Name the blood parasite species.
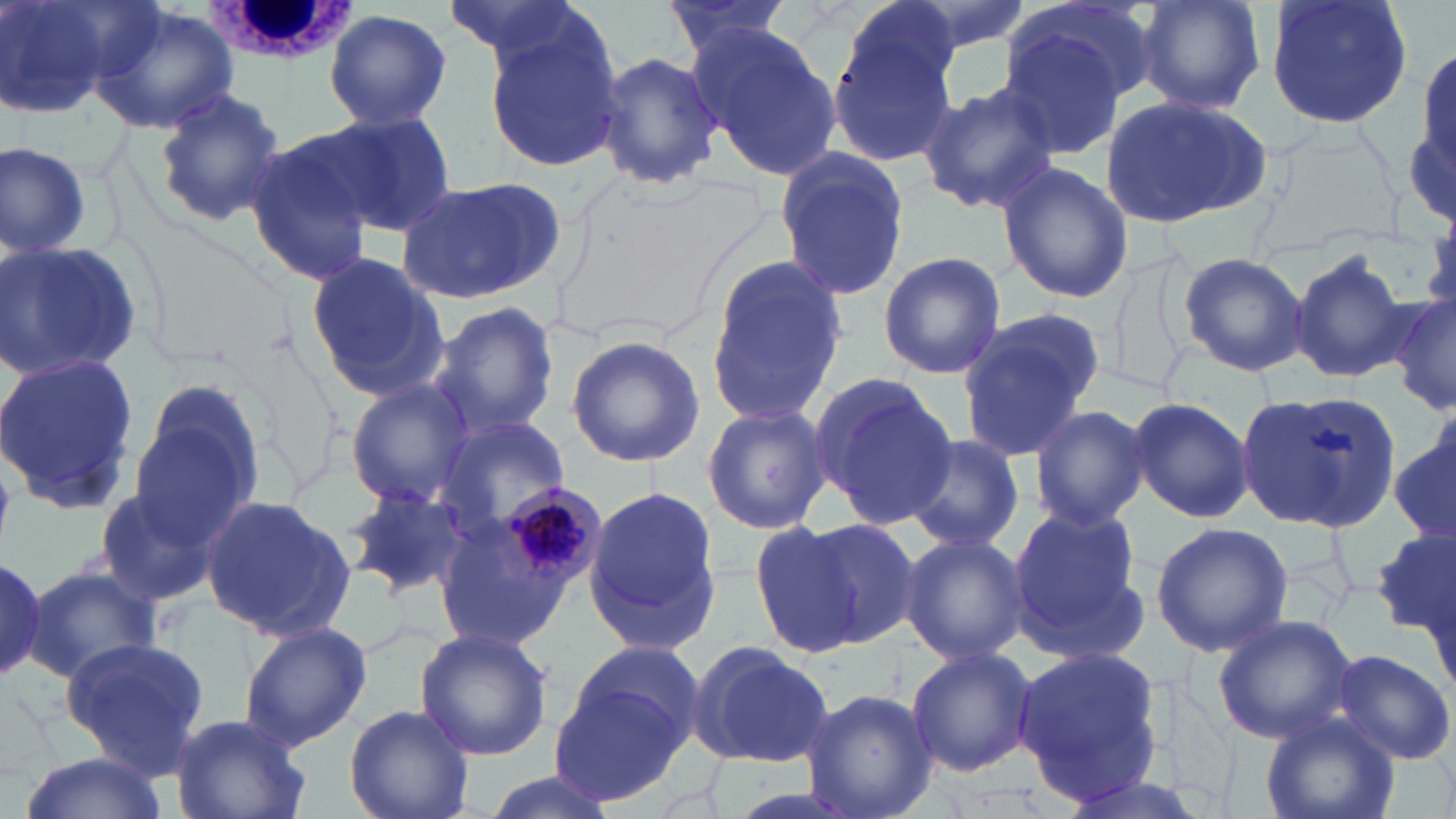
Plasmodium malariae.

Approximate bounding boxes as (x1,y1)-(x2,y2) corner pairs in pixels. Plasmodium malariae-infected red blood cell locations: (499,484)-(609,591). White blood cell locations: (200,0)-(356,67). Uninfected red blood cell locations: (0,0)-(124,120), (441,0)-(600,74), (656,0)-(799,66), (842,0)-(967,95), (881,0)-(1033,63), (1009,0)-(1156,111), (1132,0)-(1267,113), (1264,0)-(1416,131), (87,5)-(241,136), (325,9)-(452,133), (825,19)-(960,166), (688,21)-(846,180), (482,22)-(624,173), (994,23)-(1129,159), (1406,42)-(1456,232), (592,49)-(723,192), (915,83)-(1060,214), (150,87)-(286,225), (1100,95)-(1273,230), (322,109)-(461,237), (243,133)-(381,285), (1,142)-(95,261), (772,149)-(912,304), (997,162)-(1133,304), (396,176)-(566,305), (0,239)-(143,385), (1099,247)-(1199,400), (1290,249)-(1412,385), (877,250)-(1006,379), (1176,251)-(1309,376), (303,253)-(448,399), (701,256)-(845,428), (1389,293)-(1456,418), (430,301)-(560,436), (956,308)-(1105,460), (566,333)-(706,468), (0,351)-(140,514), (809,373)-(957,530), (127,375)-(268,542), (345,380)-(478,508), (1236,388)-(1398,533), (1126,396)-(1253,523), (702,401)-(833,536), (1028,404)-(1150,532), (432,416)-(570,537), (1390,430)-(1456,553), (904,434)-(1025,554), (344,484)-(475,599), (583,484)-(726,657), (95,485)-(219,607), (198,494)-(356,644), (1007,503)-(1151,662), (795,518)-(923,648), (748,520)-(866,655), (430,521)-(576,651), (1150,521)-(1294,655), (1375,529)-(1455,639), (899,533)-(1028,667), (0,552)-(47,684), (28,565)-(161,682), (1211,613)-(1357,745), (238,621)-(372,753), (413,627)-(554,761), (59,637)-(209,776), (560,639)-(708,765), (686,641)-(836,767), (906,646)-(1039,776), (1012,646)-(1165,801), (1329,648)-(1455,766), (550,680)-(690,805), (800,687)-(937,819), (344,705)-(475,819), (171,712)-(310,819), (1259,715)-(1402,819), (15,750)-(173,819), (477,771)-(625,819). May-Grünwald-Giemsa stain. Light microscopy. Captured at 1000x magnification. Image is 1456×819 pixels. Thin blood smear. One field of a larger specimen.